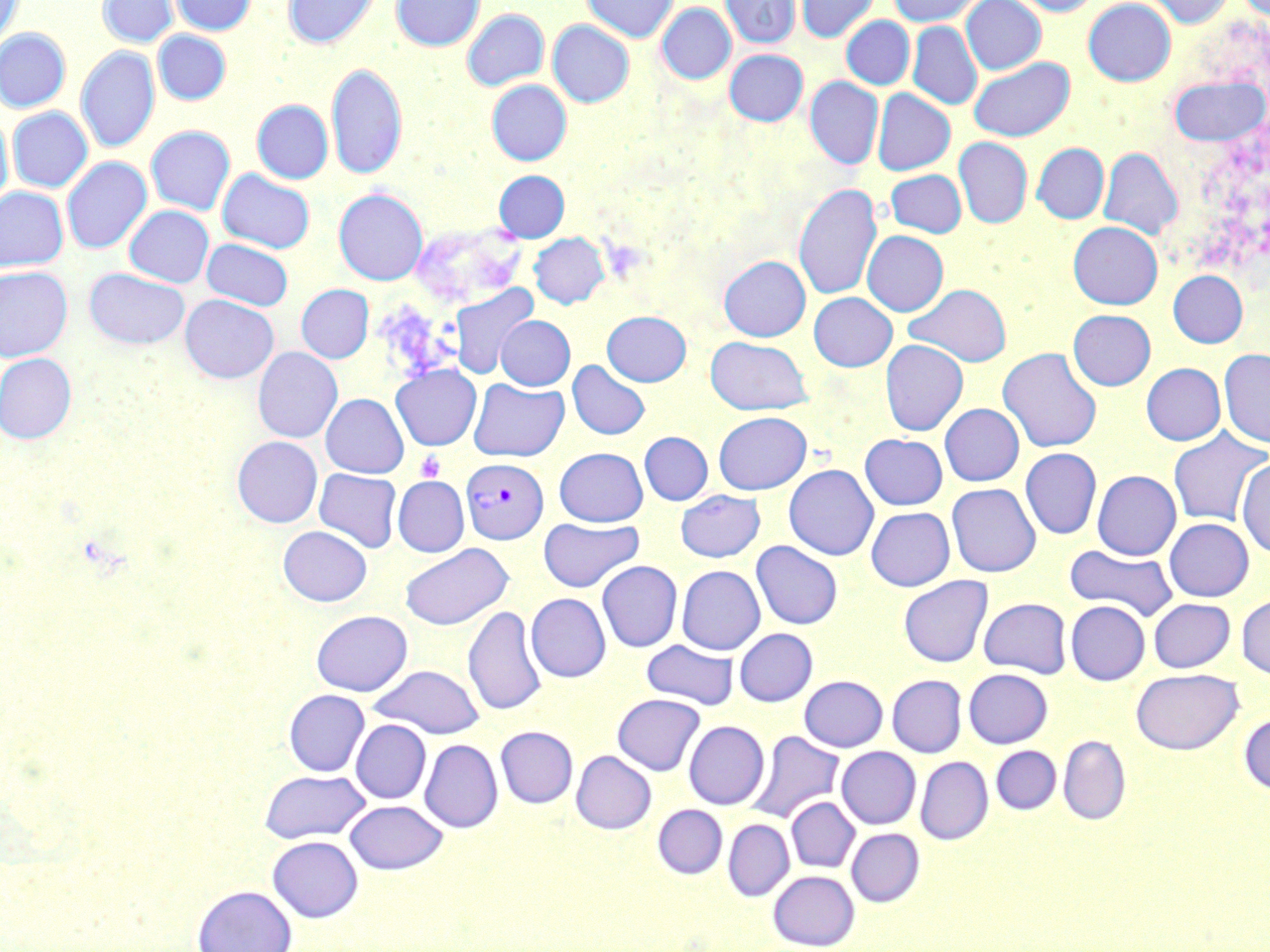

Summary:
  - Coordinate format: approximate bounding boxes as named x1/y1/x2/y2 corners in pixels
  - Platelet locations: (x1=415, y1=450, x2=445, y2=482)
  - Plasmodium vivax-infected red blood cell locations: (x1=411, y1=223, x2=526, y2=308), (x1=462, y1=458, x2=547, y2=544)
  - Uninfected red blood cell locations: (x1=0, y1=0, x2=22, y2=52), (x1=98, y1=0, x2=178, y2=47), (x1=172, y1=0, x2=256, y2=35), (x1=283, y1=0, x2=380, y2=49), (x1=392, y1=0, x2=484, y2=51), (x1=581, y1=0, x2=678, y2=42), (x1=720, y1=0, x2=800, y2=49), (x1=796, y1=0, x2=879, y2=43), (x1=888, y1=0, x2=983, y2=26), (x1=961, y1=0, x2=1046, y2=74), (x1=1012, y1=0, x2=1100, y2=16), (x1=1083, y1=0, x2=1176, y2=86), (x1=1145, y1=0, x2=1235, y2=28), (x1=657, y1=4, x2=736, y2=84), (x1=463, y1=9, x2=548, y2=91), (x1=841, y1=16, x2=914, y2=89), (x1=548, y1=20, x2=634, y2=107), (x1=908, y1=22, x2=982, y2=110), (x1=0, y1=29, x2=70, y2=112), (x1=153, y1=30, x2=231, y2=104), (x1=76, y1=46, x2=159, y2=152), (x1=725, y1=49, x2=808, y2=126), (x1=968, y1=56, x2=1075, y2=141), (x1=327, y1=62, x2=407, y2=180), (x1=1169, y1=75, x2=1268, y2=146), (x1=805, y1=77, x2=883, y2=169), (x1=487, y1=80, x2=572, y2=165), (x1=872, y1=89, x2=955, y2=175), (x1=252, y1=100, x2=333, y2=183), (x1=8, y1=107, x2=92, y2=192), (x1=0, y1=111, x2=13, y2=208), (x1=146, y1=126, x2=235, y2=214), (x1=953, y1=137, x2=1032, y2=228), (x1=1032, y1=143, x2=1109, y2=223), (x1=1099, y1=147, x2=1182, y2=240), (x1=62, y1=157, x2=151, y2=254), (x1=217, y1=168, x2=315, y2=253), (x1=885, y1=169, x2=966, y2=237), (x1=494, y1=171, x2=569, y2=242), (x1=793, y1=183, x2=882, y2=302), (x1=0, y1=187, x2=67, y2=272), (x1=334, y1=188, x2=428, y2=285), (x1=125, y1=205, x2=213, y2=287), (x1=1068, y1=221, x2=1162, y2=309), (x1=863, y1=231, x2=948, y2=316), (x1=529, y1=233, x2=609, y2=308), (x1=202, y1=239, x2=293, y2=311), (x1=719, y1=255, x2=810, y2=341), (x1=0, y1=266, x2=72, y2=361), (x1=84, y1=268, x2=190, y2=349), (x1=1168, y1=270, x2=1248, y2=347), (x1=905, y1=283, x2=1012, y2=367), (x1=296, y1=285, x2=373, y2=363), (x1=449, y1=286, x2=539, y2=380), (x1=809, y1=292, x2=897, y2=371), (x1=181, y1=295, x2=278, y2=383), (x1=1068, y1=309, x2=1155, y2=390), (x1=602, y1=311, x2=691, y2=386), (x1=495, y1=316, x2=574, y2=390), (x1=705, y1=337, x2=812, y2=415), (x1=880, y1=339, x2=968, y2=436), (x1=253, y1=347, x2=342, y2=443), (x1=998, y1=348, x2=1102, y2=453), (x1=1219, y1=348, x2=1270, y2=447), (x1=0, y1=353, x2=76, y2=444), (x1=567, y1=360, x2=650, y2=440), (x1=1141, y1=363, x2=1225, y2=445), (x1=391, y1=364, x2=481, y2=450), (x1=469, y1=378, x2=569, y2=462), (x1=321, y1=393, x2=408, y2=478), (x1=940, y1=403, x2=1024, y2=486), (x1=713, y1=411, x2=811, y2=494), (x1=1168, y1=427, x2=1269, y2=527), (x1=640, y1=432, x2=712, y2=505), (x1=860, y1=434, x2=947, y2=510), (x1=232, y1=436, x2=322, y2=527), (x1=554, y1=448, x2=648, y2=526), (x1=1020, y1=448, x2=1102, y2=539), (x1=1237, y1=459, x2=1270, y2=559), (x1=784, y1=464, x2=878, y2=560), (x1=314, y1=468, x2=401, y2=552), (x1=1092, y1=470, x2=1181, y2=560), (x1=393, y1=476, x2=469, y2=556), (x1=947, y1=483, x2=1041, y2=577), (x1=676, y1=490, x2=765, y2=562), (x1=866, y1=507, x2=955, y2=591), (x1=539, y1=517, x2=643, y2=592), (x1=1164, y1=518, x2=1254, y2=601), (x1=279, y1=525, x2=371, y2=606), (x1=751, y1=541, x2=842, y2=629), (x1=400, y1=543, x2=513, y2=630), (x1=1065, y1=544, x2=1177, y2=620), (x1=597, y1=560, x2=682, y2=652), (x1=677, y1=565, x2=765, y2=655), (x1=898, y1=575, x2=993, y2=667), (x1=526, y1=593, x2=611, y2=682), (x1=1236, y1=593, x2=1270, y2=680), (x1=979, y1=598, x2=1072, y2=678), (x1=1149, y1=598, x2=1235, y2=672), (x1=1066, y1=601, x2=1150, y2=685), (x1=463, y1=606, x2=547, y2=716), (x1=311, y1=610, x2=412, y2=695), (x1=735, y1=628, x2=818, y2=706), (x1=642, y1=639, x2=739, y2=710), (x1=368, y1=665, x2=484, y2=738), (x1=964, y1=668, x2=1053, y2=748), (x1=1131, y1=669, x2=1243, y2=755), (x1=799, y1=675, x2=887, y2=752), (x1=887, y1=675, x2=966, y2=757), (x1=283, y1=689, x2=370, y2=776), (x1=612, y1=694, x2=705, y2=775), (x1=1239, y1=712, x2=1270, y2=795), (x1=351, y1=719, x2=431, y2=803), (x1=684, y1=721, x2=769, y2=810), (x1=496, y1=726, x2=577, y2=807), (x1=750, y1=731, x2=844, y2=822), (x1=1058, y1=736, x2=1130, y2=825), (x1=419, y1=739, x2=503, y2=832), (x1=991, y1=746, x2=1061, y2=814), (x1=836, y1=747, x2=921, y2=829), (x1=571, y1=750, x2=656, y2=834), (x1=916, y1=756, x2=993, y2=845), (x1=260, y1=769, x2=369, y2=843), (x1=786, y1=796, x2=860, y2=872), (x1=345, y1=799, x2=448, y2=874), (x1=653, y1=805, x2=727, y2=878), (x1=723, y1=819, x2=794, y2=900), (x1=846, y1=828, x2=924, y2=906), (x1=267, y1=836, x2=363, y2=922), (x1=768, y1=870, x2=859, y2=949), (x1=193, y1=885, x2=297, y2=952)
  - Slide-level diagnosis: Plasmodium vivax
  - Stain: May-Grünwald-Giemsa
  - Preparation: thin blood smear
  - Image size: 1270×952 pixels
  - Field of view: single
  - Modality: optical microscopy
  - Magnification: 1000x